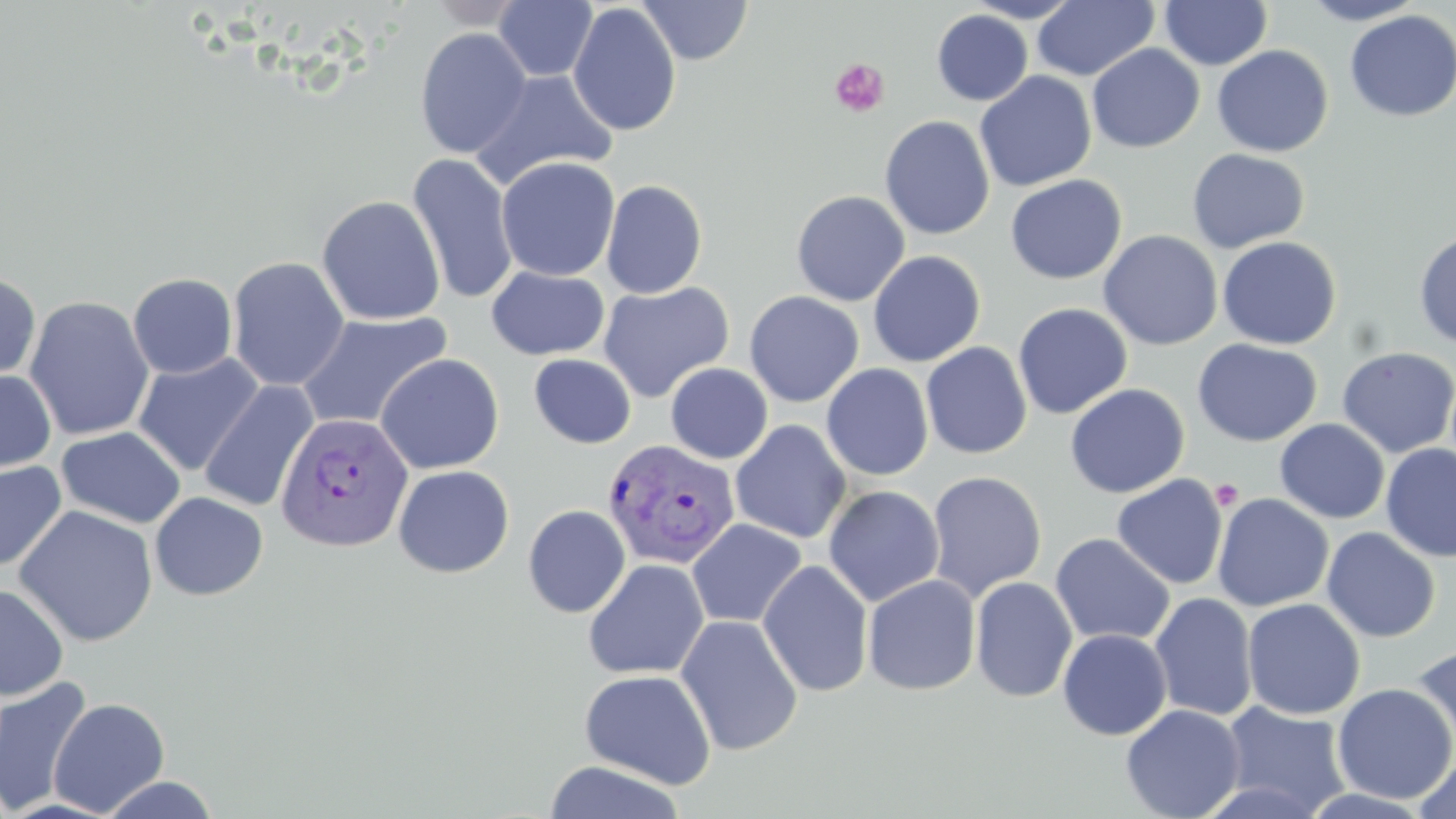 Approximate bounding boxes as (x1,y1)-(x2,y2) corner pairs in pixels. Uninfected red blood cell locations: (637,0)-(753,65), (962,0)-(1084,23), (1032,0)-(1159,81), (1159,0)-(1272,70), (1298,0)-(1428,25), (423,1)-(529,29), (493,1)-(597,82), (568,2)-(682,137), (931,10)-(1033,106), (1344,10)-(1456,122), (414,27)-(533,159), (1086,43)-(1205,153), (1212,45)-(1333,157), (470,69)-(618,191), (975,71)-(1096,191), (879,114)-(995,240), (1186,148)-(1310,253), (406,154)-(520,305), (496,156)-(620,281), (1005,174)-(1127,284), (600,179)-(708,299), (791,189)-(911,306), (317,195)-(445,326), (1413,228)-(1456,348), (1098,230)-(1223,350), (1216,237)-(1341,350), (867,249)-(986,367), (227,257)-(349,391), (486,266)-(610,360), (0,270)-(41,387), (127,272)-(237,379), (597,281)-(735,403), (744,290)-(864,407), (23,295)-(155,441), (1012,303)-(1132,419), (295,311)-(453,432), (1192,338)-(1322,447), (921,342)-(1032,459), (1337,346)-(1456,458), (1363,347)-(1456,565), (132,353)-(265,476), (374,353)-(504,474), (529,354)-(636,448), (665,363)-(773,464), (821,363)-(934,481), (0,369)-(57,476), (199,380)-(319,513), (1065,383)-(1189,499), (1274,419)-(1390,524), (731,420)-(851,544), (56,425)-(186,529), (42,428)-(179,635), (1380,443)-(1456,562), (0,461)-(67,572), (393,464)-(514,578), (926,470)-(1047,601), (1111,474)-(1228,590), (823,485)-(944,607), (150,491)-(268,601), (1212,493)-(1334,612), (13,505)-(159,647), (522,505)-(631,618), (686,518)-(807,629), (1321,527)-(1440,643), (1050,533)-(1175,647), (9,546)-(114,687), (583,559)-(709,680), (758,560)-(874,698), (863,574)-(981,695), (970,576)-(1078,703), (0,583)-(69,700), (1150,592)-(1258,722), (1242,598)-(1365,719), (676,614)-(803,756), (1058,628)-(1172,740), (1409,643)-(1456,760), (579,668)-(716,789), (0,676)-(94,816), (1332,683)-(1456,804), (48,698)-(170,816), (1218,701)-(1353,818), (1121,704)-(1245,819), (1414,752)-(1456,819), (543,761)-(687,819), (97,775)-(221,818). Platelet locations: (829,57)-(889,117), (1209,479)-(1244,510). Plasmodium vivax-infected red blood cell locations: (275,411)-(414,552), (603,438)-(741,570). Slide-level diagnosis: Plasmodium vivax. Thin blood smear. Captured at 1000x magnification. Single field of view. Optical microscopy. May-Grünwald-Giemsa-stained preparation. Image is 1456×819 pixels.